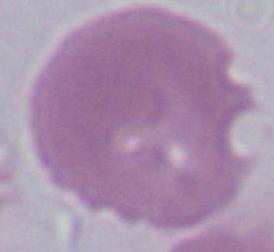

Summary:
  - Magnification: 1000x
  - Identification: red blood cell
  - Modality: micrograph